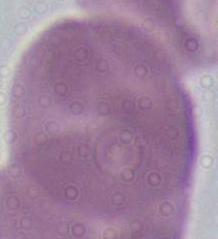

Micrograph. A red blood cell is seen. 1000x magnification.